Assess the morphology of the erythrocytes.
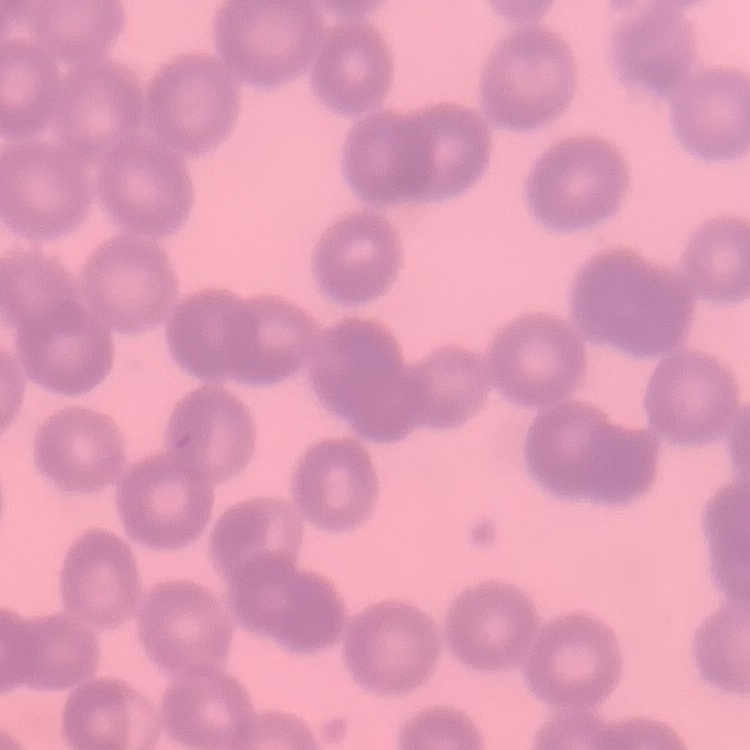

No rouleaux formation.

Summary:
  - Stain: Field's or Giemsa
  - Image type: square crop of a larger photomicrograph
  - Preparation: thin peripheral smear